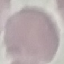

Summary:
  - Malaria status: uninfected
  - Preparation: thin smear
  - Stain: Giemsa
  - Image type: cell patch, automatically extracted from a larger field of view and resized to 64 × 64 pixels
  - Capture: smartphone through the microscope eyepiece